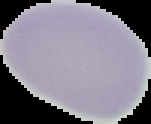 From a thin blood smear. Image is 151×124 pixels. The area outside the segmented cell region is set to black. Malaria status: uninfected.